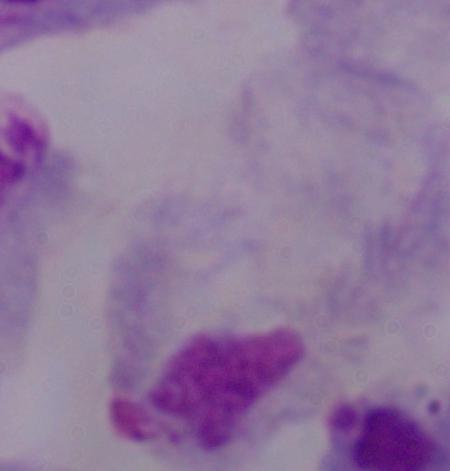

Summary:
  - Magnification: 1000x
  - Identification: trichomonad
  - Modality: photomicrograph